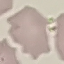

result = no malaria parasites detected
preparation = thin blood film
image type = cell patch, automatically extracted from a larger field of view and resized to 64 × 64 pixels
capture = smartphone through the microscope eyepiece
stain = Giemsa